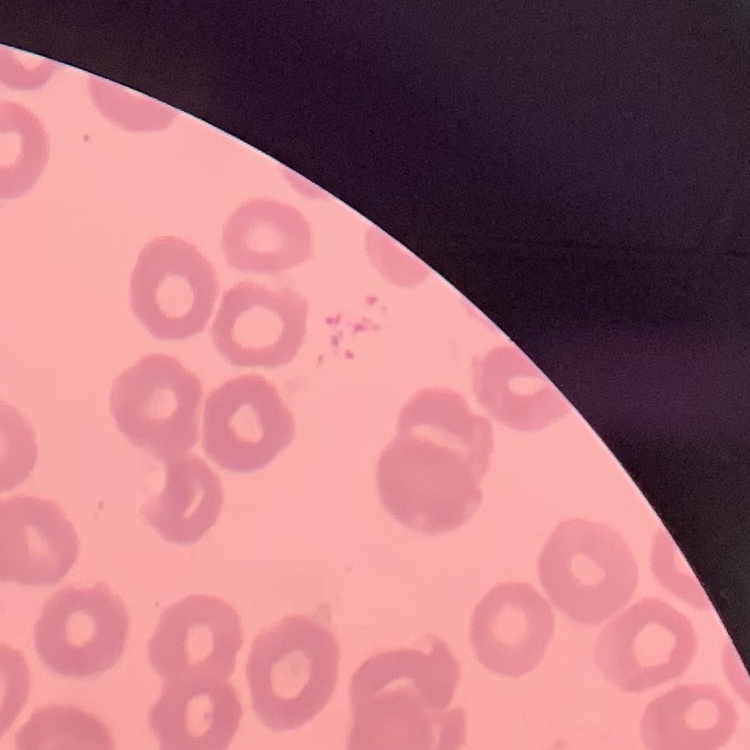

The erythrocytes show no rouleaux formation. Stained with either Field's or Giemsa. One tile cut from a larger photomicrograph. Thin peripheral smear.